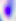
Micrograph. 400x magnification. Toxoplasma gondii is shown.